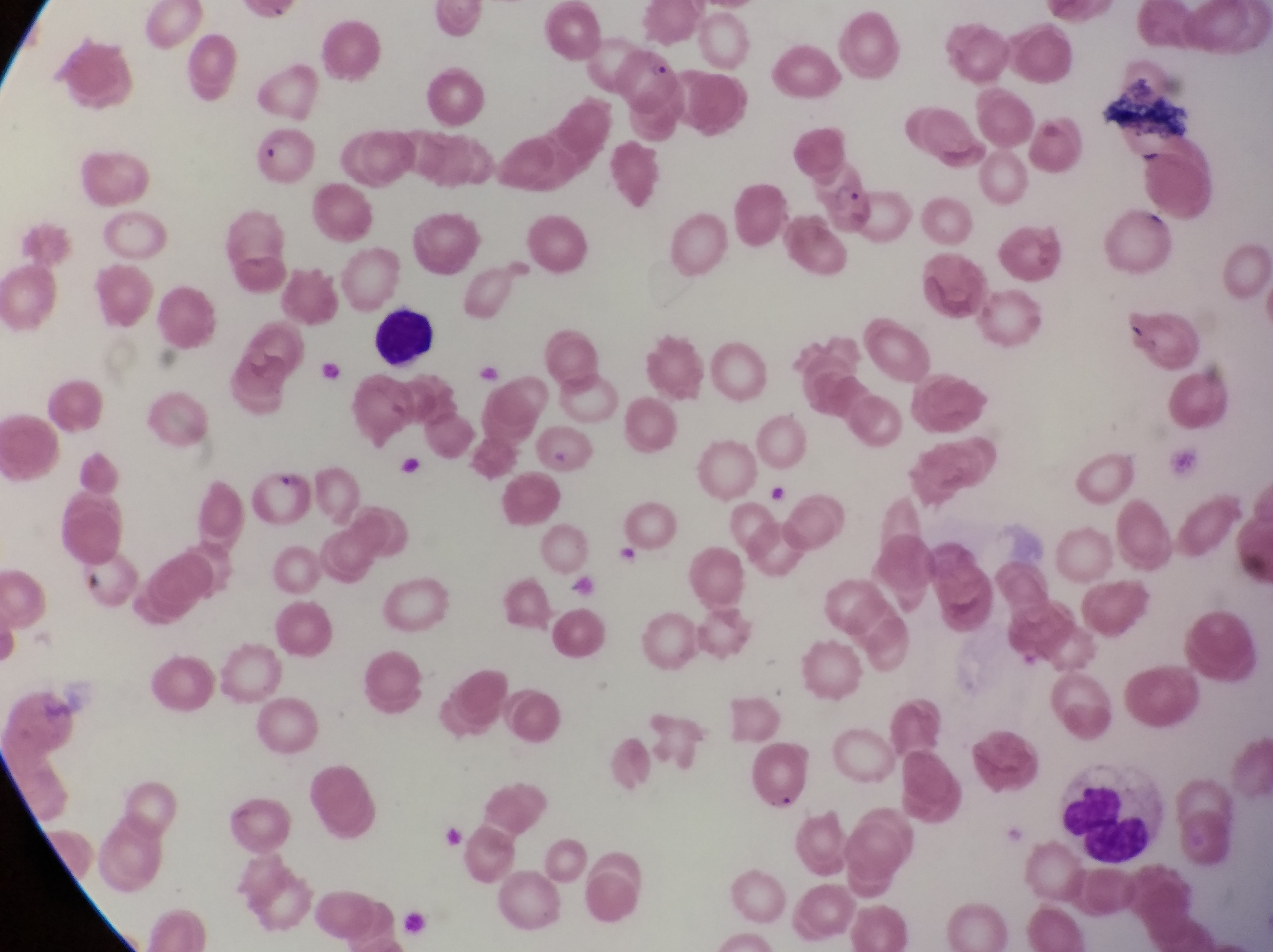
Approximate bounding boxes as [left, top, right, bottom] in pixels.
Summary:
  - Parasitised red blood cell locations: [816, 175, 883, 242], [252, 462, 315, 536]
  - Artifact (platelet-like body, stain precipitate, or debris) locations: [544, 442, 576, 481]
  - Leukocyte locations: [370, 297, 442, 375], [1053, 756, 1150, 864]
  - Country: Uganda
  - Capture: smartphone photograph through the eyepiece of an Olympus CX-23 microscope
  - Image size: 1273×952 pixels
  - Magnification: 1000x
  - Field of view: single
  - Preparation: thin blood smear